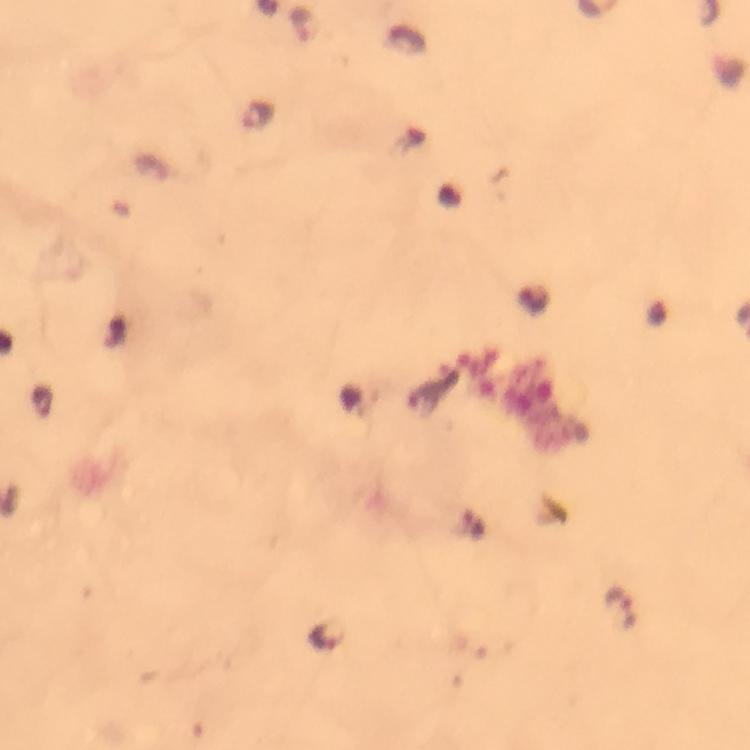

Approximate centers as (x, y) in pixels.
Summary:
  - Malaria parasite locations: (303, 25), (258, 115), (619, 608), (327, 635)
  - Preparation: thick smear
  - Immersion oil: applied
  - Context: from a diagnostic examination for malaria
  - Stain: Giemsa
  - Magnification: 100x
  - Cropped from: one field of view
  - Capture: smartphone camera through the microscope
  - Image size: 750×750 pixels